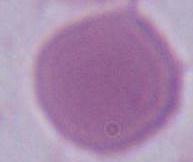

Summary:
  - Modality: micrograph
  - Magnification: 1000x
  - Identification: red blood cell